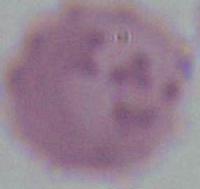

Summary:
  - Magnification: 1000x
  - Identification: red blood cell
  - Modality: micrograph